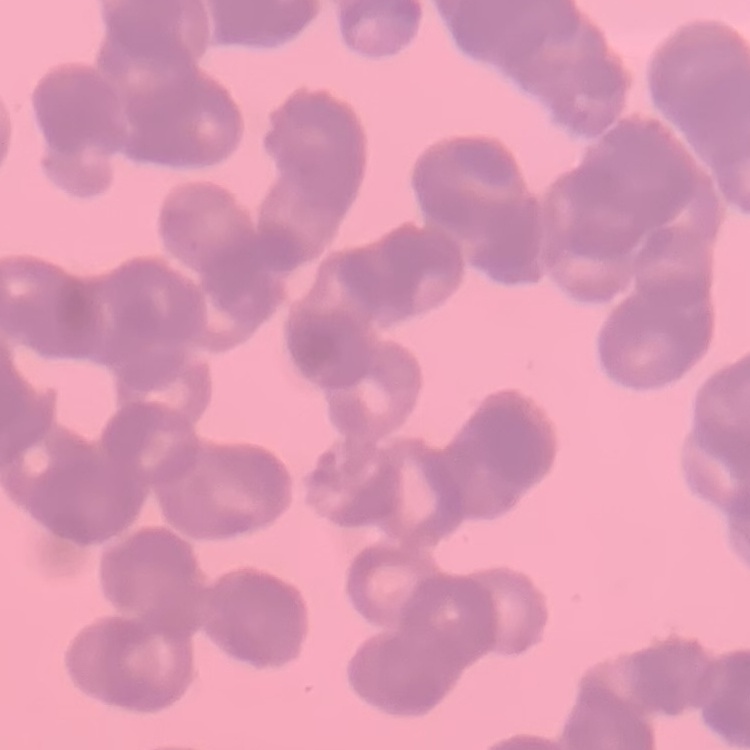

erythrocyte morphology = rouleaux formation
stain = Field's or Giemsa
preparation = thin peripheral smear
image type = square crop of a larger photomicrograph